Locate and identify every blood parasite.
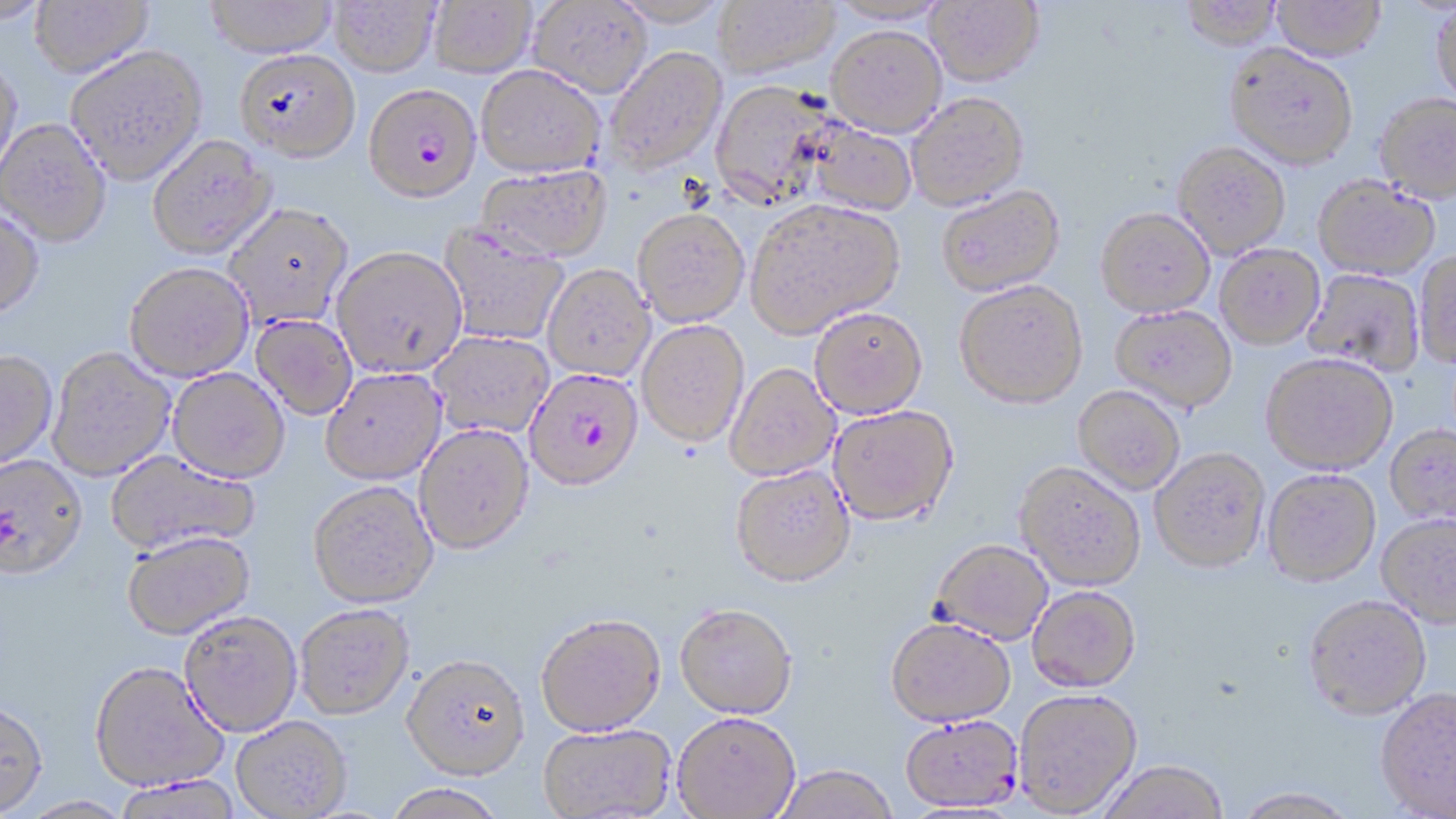

Approximate bounding boxes as named x1/y1/x2/y2 corners in pixels.
Plasmodium falciparum-infected red blood cells: (x1=363, y1=83, x2=480, y2=203), (x1=526, y1=369, x2=645, y2=494), (x1=900, y1=718, x2=1025, y2=815).
No Plasmodium ovale, Plasmodium malariae, Plasmodium vivax, Babesia divergens, or Trypanosoma brucei observed.

slide-level diagnosis = Plasmodium falciparum
modality = light microscopy
magnification = 1000x
image size = 1456×819 pixels
field of view = one of a larger specimen
preparation = thin blood film
uninfected red blood cell locations = approximate bounding boxes as named x1/y1/x2/y2 corners in pixels: (x1=0, y1=0, x2=54, y2=26), (x1=29, y1=0, x2=154, y2=78), (x1=204, y1=0, x2=338, y2=58), (x1=329, y1=0, x2=440, y2=77), (x1=428, y1=0, x2=537, y2=77), (x1=611, y1=0, x2=727, y2=27), (x1=713, y1=0, x2=840, y2=80), (x1=827, y1=0, x2=952, y2=25), (x1=926, y1=0, x2=1044, y2=85), (x1=1180, y1=0, x2=1284, y2=51), (x1=527, y1=1, x2=653, y2=97), (x1=1271, y1=1, x2=1386, y2=62), (x1=1431, y1=4, x2=1456, y2=107), (x1=826, y1=25, x2=946, y2=136), (x1=1225, y1=45, x2=1358, y2=170), (x1=65, y1=46, x2=208, y2=184), (x1=603, y1=46, x2=727, y2=174), (x1=235, y1=48, x2=361, y2=161), (x1=0, y1=56, x2=24, y2=187), (x1=476, y1=65, x2=606, y2=178), (x1=708, y1=79, x2=835, y2=209), (x1=907, y1=92, x2=1029, y2=210), (x1=1374, y1=94, x2=1456, y2=203), (x1=0, y1=118, x2=112, y2=247), (x1=802, y1=119, x2=917, y2=216), (x1=147, y1=135, x2=276, y2=260), (x1=1173, y1=142, x2=1291, y2=259), (x1=474, y1=165, x2=611, y2=262), (x1=1314, y1=178, x2=1440, y2=282), (x1=937, y1=186, x2=1065, y2=297), (x1=746, y1=199, x2=905, y2=339), (x1=224, y1=204, x2=353, y2=329), (x1=0, y1=208, x2=45, y2=321), (x1=633, y1=208, x2=750, y2=327), (x1=1095, y1=209, x2=1215, y2=319), (x1=438, y1=224, x2=569, y2=346), (x1=1215, y1=246, x2=1325, y2=351), (x1=331, y1=247, x2=467, y2=379), (x1=1414, y1=252, x2=1456, y2=369), (x1=124, y1=263, x2=254, y2=383), (x1=542, y1=264, x2=654, y2=383), (x1=1303, y1=270, x2=1423, y2=377), (x1=954, y1=283, x2=1088, y2=410), (x1=1110, y1=306, x2=1237, y2=414), (x1=810, y1=309, x2=929, y2=420), (x1=251, y1=316, x2=357, y2=421), (x1=637, y1=321, x2=750, y2=449), (x1=430, y1=332, x2=554, y2=439), (x1=46, y1=348, x2=176, y2=483), (x1=0, y1=352, x2=58, y2=473), (x1=1261, y1=356, x2=1397, y2=478), (x1=725, y1=365, x2=840, y2=483), (x1=167, y1=370, x2=290, y2=486), (x1=320, y1=370, x2=447, y2=487), (x1=1073, y1=387, x2=1185, y2=496), (x1=829, y1=407, x2=959, y2=530), (x1=414, y1=425, x2=535, y2=558), (x1=1385, y1=426, x2=1456, y2=528), (x1=1149, y1=451, x2=1271, y2=576), (x1=105, y1=452, x2=259, y2=558), (x1=0, y1=457, x2=89, y2=585), (x1=1014, y1=465, x2=1145, y2=594), (x1=730, y1=468, x2=855, y2=591), (x1=1262, y1=472, x2=1381, y2=590), (x1=308, y1=484, x2=439, y2=611), (x1=1376, y1=516, x2=1456, y2=629), (x1=121, y1=534, x2=256, y2=643), (x1=930, y1=542, x2=1053, y2=647), (x1=1027, y1=589, x2=1140, y2=695), (x1=1303, y1=599, x2=1432, y2=724), (x1=295, y1=607, x2=415, y2=723), (x1=674, y1=608, x2=797, y2=722), (x1=179, y1=614, x2=302, y2=740), (x1=536, y1=618, x2=666, y2=741), (x1=885, y1=622, x2=1016, y2=731), (x1=401, y1=658, x2=531, y2=785), (x1=88, y1=665, x2=229, y2=795), (x1=1375, y1=690, x2=1456, y2=818), (x1=1014, y1=692, x2=1142, y2=818), (x1=0, y1=704, x2=49, y2=818), (x1=673, y1=716, x2=800, y2=819), (x1=231, y1=719, x2=353, y2=818), (x1=538, y1=726, x2=675, y2=819), (x1=1099, y1=763, x2=1228, y2=819), (x1=775, y1=768, x2=898, y2=819), (x1=113, y1=777, x2=243, y2=819), (x1=383, y1=786, x2=507, y2=819), (x1=1233, y1=790, x2=1358, y2=818), (x1=20, y1=797, x2=136, y2=819)
stain = May-Grünwald-Giemsa